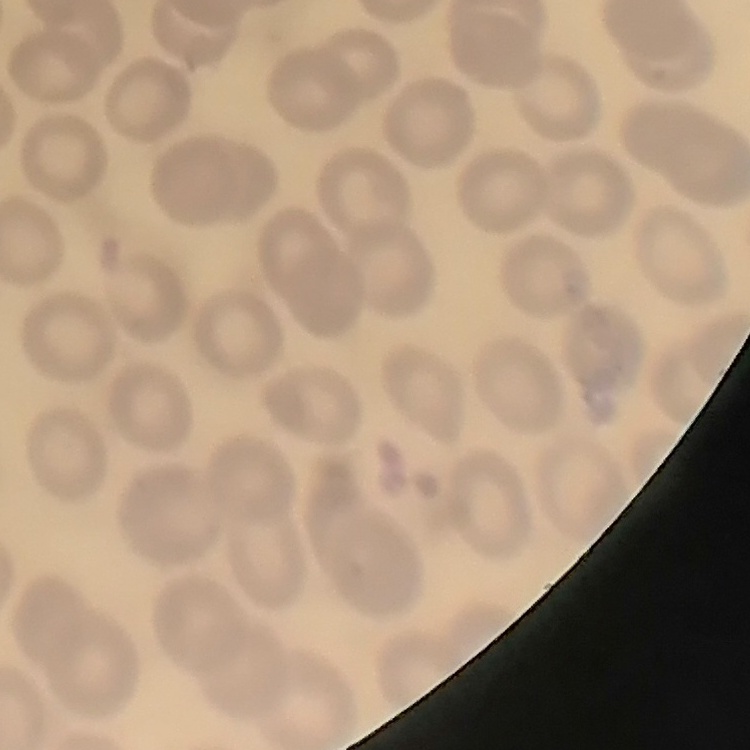

Summary:
  - Red blood cell morphology: no rouleaux formation
  - Image type: one tile cut from a larger photomicrograph
  - Stain: Field's or Giemsa
  - Preparation: thin blood film